Give the preparation type.
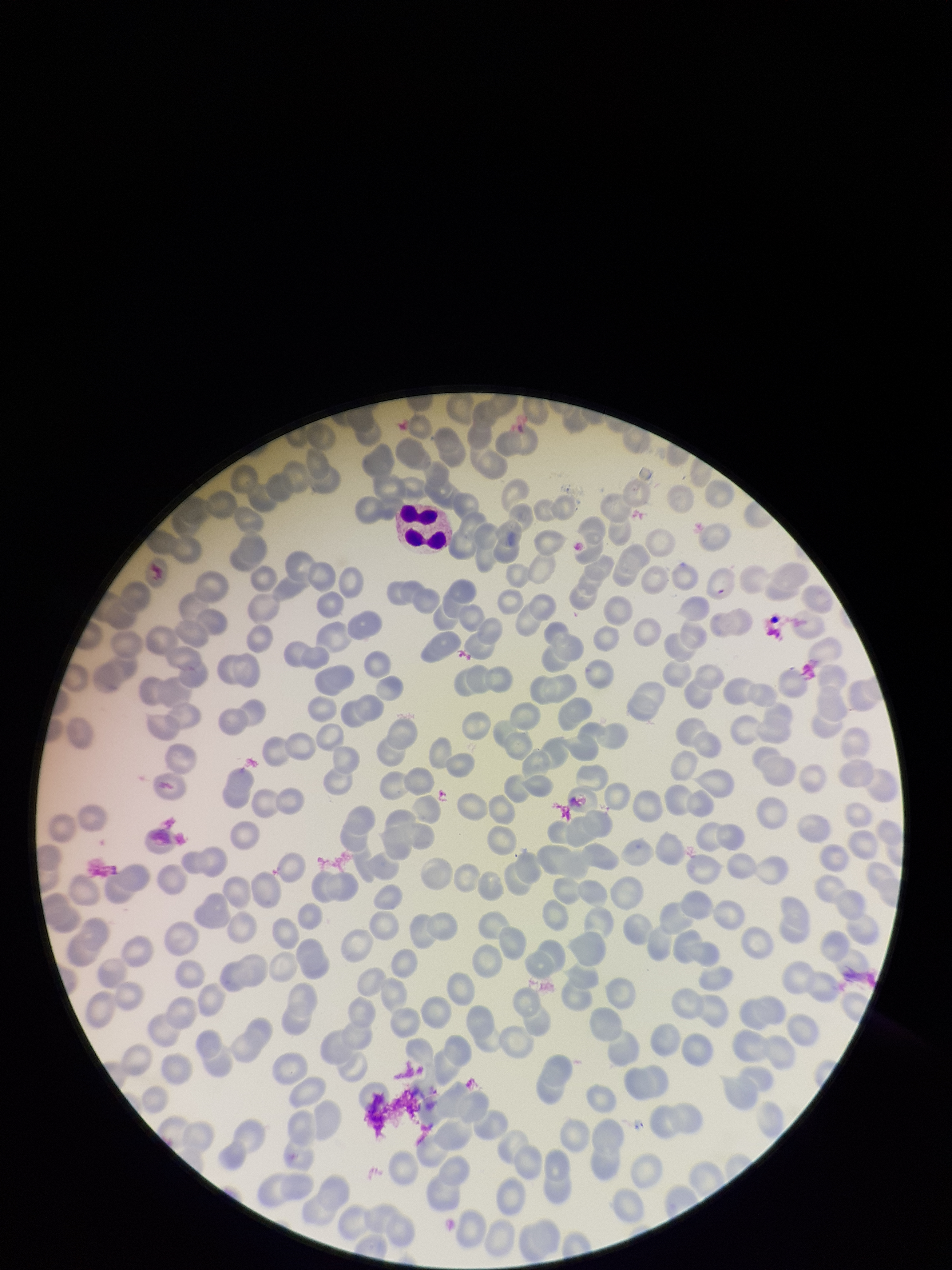
Thin.

{
  "capture": "smartphone photograph through the microscope eyepiece",
  "parasitized_red_blood_cell_count": 0,
  "field_of_view": "one from this slide",
  "image_size": "952×1270 pixels",
  "patient_malaria_status": "negative",
  "stain": "Giemsa",
  "parasitized_red_blood_cells": "none identified",
  "red_blood_cell_count": 213
}